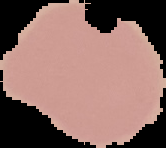
image size = 166×148 pixels
image type = segmented cell region with the area outside set to black
preparation = thin blood smear
result = no malaria parasites detected